Name the cell type shown.
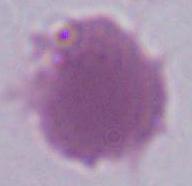

This is an erythrocyte.

Photomicrograph. Captured at 1000x magnification.